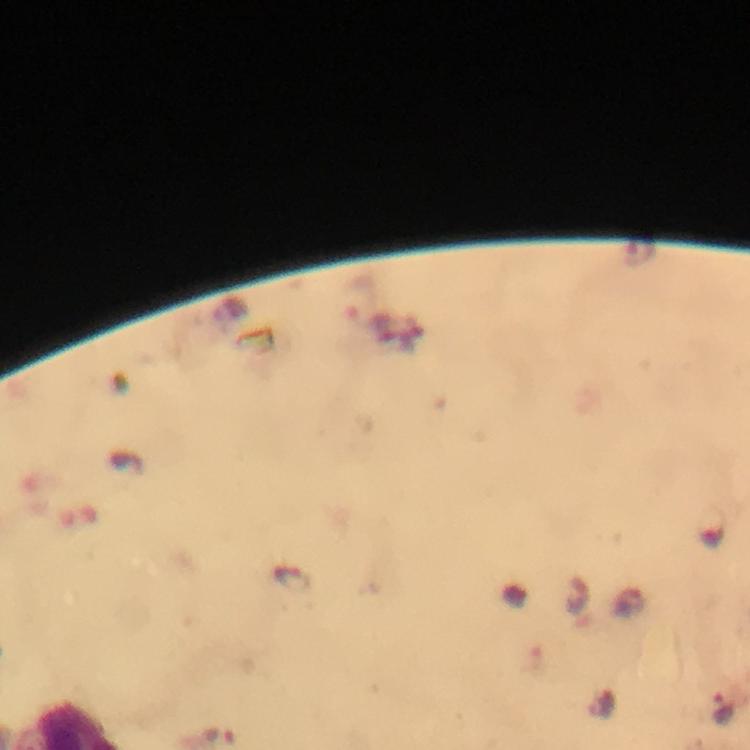
Approximate object centers, in pixels from the top-left corner.
Summary:
  - Plasmodium parasite locations: (x=360, y=298), (x=294, y=580), (x=722, y=710)
  - Cropped from: one field of view
  - Context: from a diagnostic examination for malaria
  - Stain: Giemsa
  - Image size: 750×750 pixels
  - Capture: smartphone mounted on the microscope
  - Preparation: thick blood smear
  - Immersion oil: used
  - Magnification: 100x